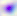

magnification = 400x
identification = Toxoplasma gondii
modality = photomicrograph